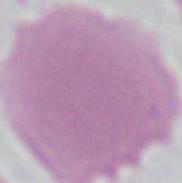

identification = erythrocyte
modality = micrograph
magnification = 1000x